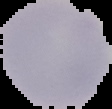

Summary:
  - Result: negative for malaria parasites
  - Image type: segmented cell region on a black background
  - Image size: 112×109 pixels
  - Preparation: thin blood film